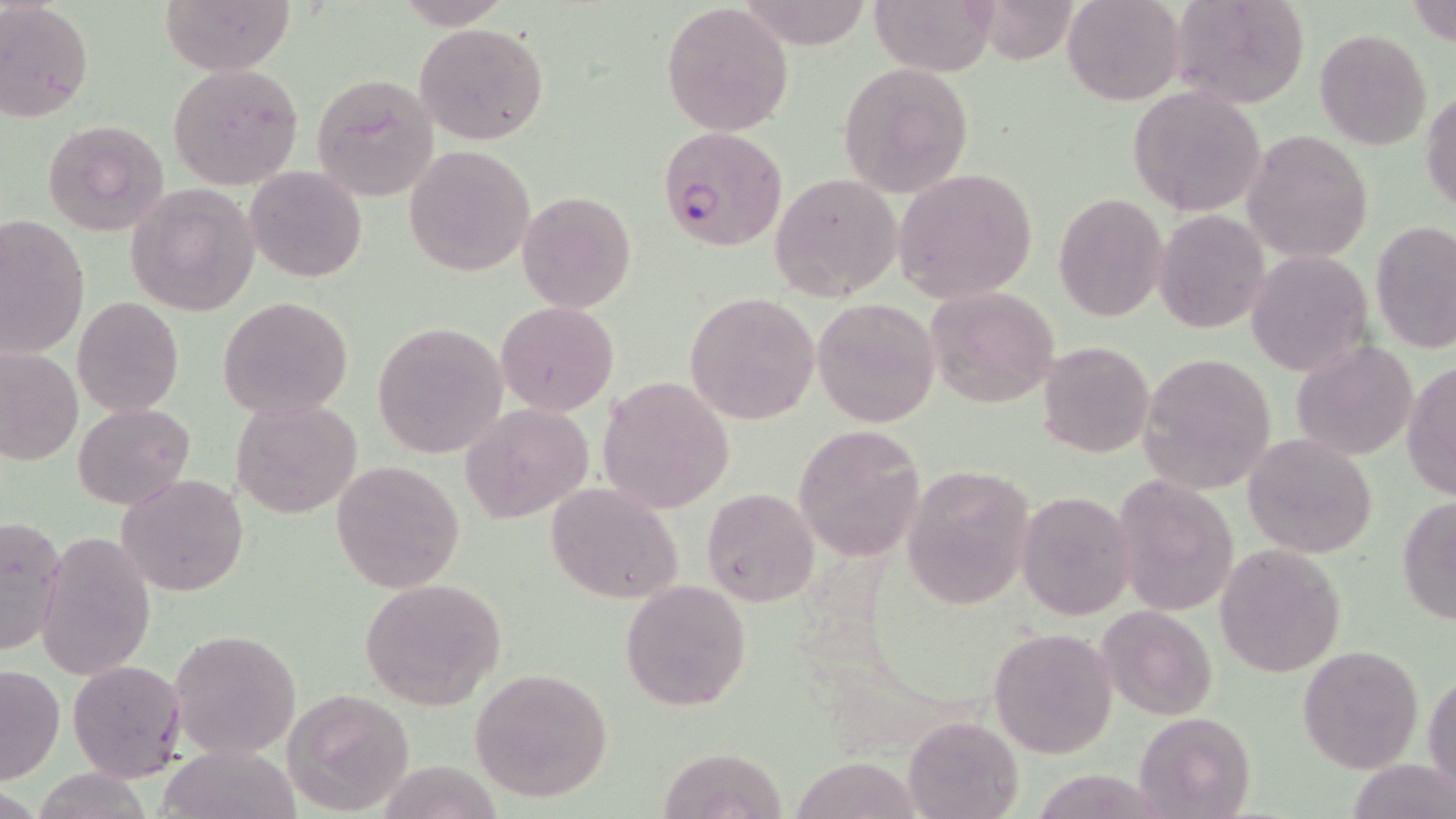

slide_level_diagnosis: Plasmodium falciparum
uninfected_red_blood_cell_locations: 'approximate bounding boxes as (x1, y1, x2, y2) in pixels: (161, 0, 294, 75), (392, 0, 515, 28), (869, 0, 996, 75), (1061, 0, 1184, 106), (1168, 0, 1312, 111), (1407, 0, 1456, 46), (0, 1, 95, 123), (661, 3, 794, 138), (413, 22, 550, 146), (1315, 29, 1431, 150), (168, 62, 304, 192), (835, 62, 974, 197), (310, 74, 439, 201), (1125, 85, 1269, 217), (1422, 89, 1455, 215), (41, 119, 170, 237), (1243, 129, 1372, 265), (403, 146, 536, 277), (244, 166, 366, 282), (893, 168, 1039, 304), (770, 172, 903, 303), (125, 184, 258, 317), (517, 191, 636, 312), (1053, 192, 1169, 323), (1153, 211, 1270, 332), (1, 214, 92, 358), (1371, 220, 1456, 354), (1246, 249, 1373, 378), (925, 287, 1060, 407), (685, 293, 821, 424), (71, 296, 184, 418), (217, 296, 355, 420), (812, 297, 942, 429), (495, 302, 619, 416), (371, 322, 510, 457), (1039, 340, 1154, 458), (1292, 342, 1419, 461), (0, 347, 82, 465), (1138, 351, 1278, 494), (1402, 361, 1456, 501), (597, 376, 735, 514), (232, 398, 363, 520), (73, 402, 194, 510), (461, 403, 592, 525), (792, 424, 925, 563), (1242, 434, 1378, 558), (331, 459, 464, 594), (902, 466, 1034, 608), (117, 473, 249, 597), (1112, 475, 1238, 617), (545, 483, 684, 604), (701, 487, 819, 608), (1016, 491, 1135, 619), (1396, 496, 1456, 625), (0, 516, 66, 657), (36, 533, 155, 680), (1215, 544, 1346, 679), (358, 578, 506, 710), (620, 579, 752, 712), (1098, 604, 1217, 721), (989, 626, 1118, 759), (168, 629, 301, 761), (1297, 643, 1423, 774), (67, 659, 186, 782), (0, 663, 65, 787), (468, 667, 613, 802), (1424, 670, 1455, 801), (282, 688, 416, 814), (1133, 710, 1255, 819), (902, 715, 1022, 819), (162, 744, 299, 819), (656, 747, 784, 818), (792, 756, 922, 819)'
field_of_view: single
modality: light microscopy
image_size: 1456×819 pixels
plasmodium_falciparum_infected_red_blood_cell_locations: 'approximate bounding boxes as (x1, y1, x2, y2) in pixels: (655, 126, 787, 251)'
preparation: thin blood smear
stain: May-Grünwald-Giemsa
magnification: 1000x